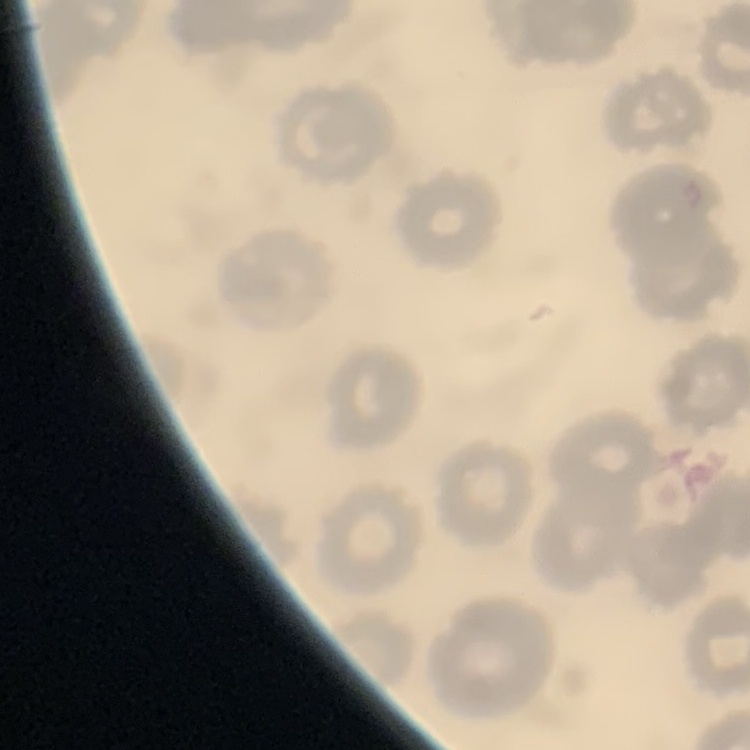
The red blood cells exhibit no rouleaux formation. One tile cut from a larger photomicrograph. Field's or Giemsa stain. Thin blood film.